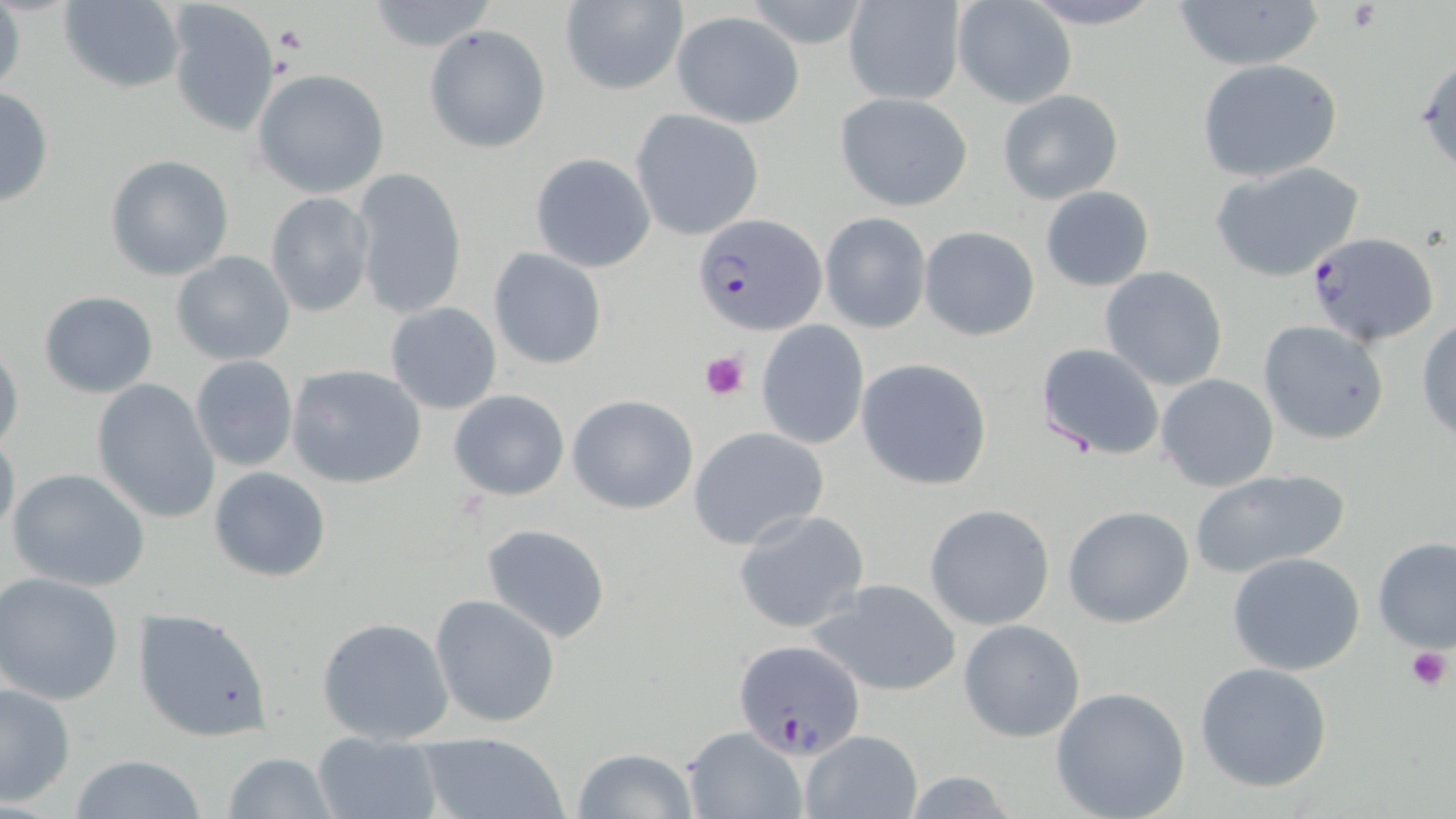

slide_level_diagnosis: Plasmodium falciparum
preparation: thin blood smear
stain: May-Grünwald-Giemsa
plasmodium_falciparum_infected_red_blood_cell_locations: 'approximate bounding boxes as named x1/y1/x2/y2 corners in pixels: (x1=693, y1=212, x2=827, y2=336), (x1=1302, y1=231, x2=1440, y2=347), (x1=734, y1=637, x2=865, y2=758)'
modality: light microscopy
platelet_locations: 'approximate bounding boxes as named x1/y1/x2/y2 corners in pixels: (x1=700, y1=350, x2=748, y2=400), (x1=1406, y1=645, x2=1453, y2=690)'
field_of_view: single
magnification: 1000x
image_size: 1456×819 pixels
uninfected_red_blood_cell_locations: 'approximate bounding boxes as named x1/y1/x2/y2 corners in pixels: (x1=0, y1=0, x2=24, y2=99), (x1=59, y1=0, x2=187, y2=92), (x1=165, y1=0, x2=281, y2=137), (x1=740, y1=0, x2=877, y2=51), (x1=952, y1=0, x2=1077, y2=108), (x1=1017, y1=0, x2=1168, y2=28), (x1=365, y1=1, x2=497, y2=52), (x1=557, y1=1, x2=688, y2=97), (x1=1172, y1=1, x2=1325, y2=72), (x1=843, y1=3, x2=965, y2=105), (x1=672, y1=11, x2=804, y2=127), (x1=425, y1=24, x2=552, y2=153), (x1=1413, y1=51, x2=1456, y2=173), (x1=1196, y1=59, x2=1344, y2=183), (x1=251, y1=69, x2=390, y2=198), (x1=0, y1=86, x2=53, y2=209), (x1=997, y1=88, x2=1123, y2=204), (x1=835, y1=92, x2=973, y2=209), (x1=631, y1=110, x2=764, y2=240), (x1=530, y1=153, x2=655, y2=272), (x1=103, y1=154, x2=235, y2=281), (x1=1209, y1=161, x2=1366, y2=282), (x1=352, y1=165, x2=467, y2=319), (x1=1039, y1=186, x2=1153, y2=292), (x1=264, y1=192, x2=375, y2=316), (x1=819, y1=212, x2=931, y2=334), (x1=919, y1=226, x2=1040, y2=342), (x1=489, y1=248, x2=607, y2=370), (x1=171, y1=250, x2=295, y2=365), (x1=1099, y1=266, x2=1229, y2=391), (x1=38, y1=291, x2=159, y2=398), (x1=385, y1=302, x2=502, y2=414), (x1=1415, y1=317, x2=1456, y2=442), (x1=1256, y1=320, x2=1391, y2=445), (x1=756, y1=321, x2=869, y2=449), (x1=0, y1=342, x2=24, y2=455), (x1=1035, y1=342, x2=1165, y2=461), (x1=190, y1=355, x2=298, y2=471), (x1=856, y1=358, x2=992, y2=490), (x1=285, y1=364, x2=425, y2=489), (x1=1155, y1=373, x2=1280, y2=492), (x1=90, y1=379, x2=220, y2=525), (x1=448, y1=389, x2=571, y2=500), (x1=568, y1=394, x2=698, y2=513), (x1=687, y1=427, x2=830, y2=550), (x1=0, y1=429, x2=20, y2=542), (x1=6, y1=467, x2=151, y2=592), (x1=209, y1=467, x2=331, y2=582), (x1=1187, y1=468, x2=1351, y2=578), (x1=924, y1=504, x2=1054, y2=630), (x1=1063, y1=505, x2=1195, y2=629), (x1=733, y1=509, x2=869, y2=634), (x1=480, y1=523, x2=613, y2=643), (x1=1373, y1=538, x2=1456, y2=655), (x1=1227, y1=553, x2=1367, y2=676), (x1=0, y1=573, x2=125, y2=704), (x1=808, y1=577, x2=964, y2=697), (x1=429, y1=593, x2=562, y2=728), (x1=133, y1=608, x2=274, y2=743), (x1=317, y1=616, x2=454, y2=744), (x1=958, y1=618, x2=1086, y2=743), (x1=1194, y1=662, x2=1333, y2=792), (x1=0, y1=679, x2=76, y2=808), (x1=1049, y1=685, x2=1191, y2=819), (x1=681, y1=726, x2=806, y2=818), (x1=800, y1=730, x2=920, y2=818), (x1=312, y1=731, x2=443, y2=819), (x1=417, y1=731, x2=570, y2=819), (x1=573, y1=748, x2=699, y2=819), (x1=224, y1=752, x2=338, y2=819), (x1=67, y1=755, x2=212, y2=818)'